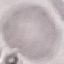 Result: no malaria parasites seen. Giemsa-stained preparation. Thin blood smear. Cell patch, automatically extracted from a larger field of view and resized to 64 × 64 pixels. Photographed with a smartphone camera at the microscope eyepiece.